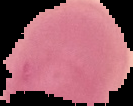 From a thin blood film. Image is 133×106 pixels. Result: no malaria parasites detected. The area outside the segmented cell region is set to black.